Assess this cell for malaria.
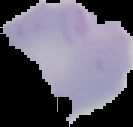
Parasitized.

image type = cell region segmented out of the field of view; surrounding area masked to black
preparation = thin blood smear
image size = 133×127 pixels